Name the cell type shown.
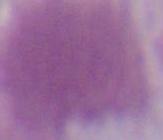

An erythrocyte.

Captured at 1000x magnification. Photomicrograph.